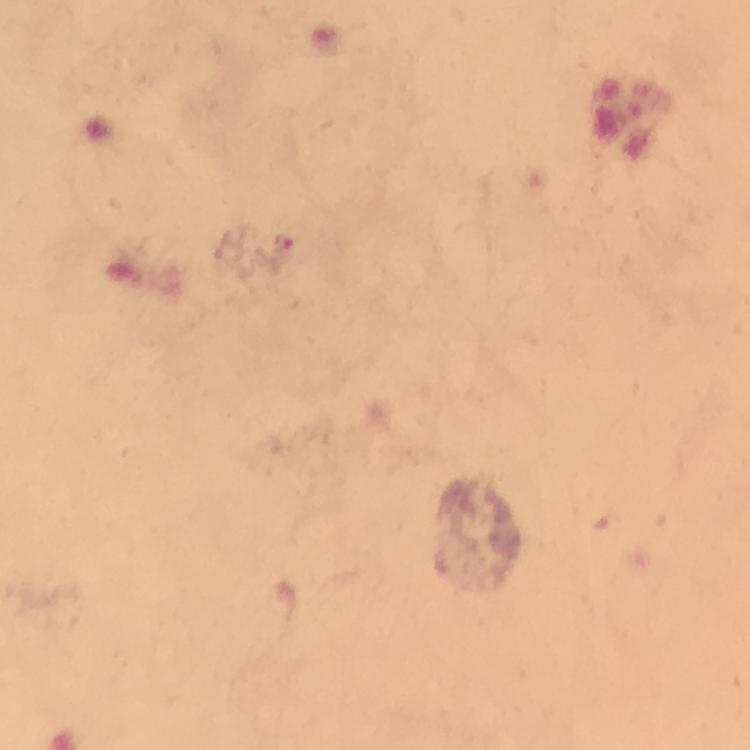

context = from a diagnostic examination for malaria
capture = smartphone photograph through a microscope
preparation = thick blood smear
magnification = 100x
cropped from = one field of view
image size = 750×750 pixels
malaria parasite locations = approximate object centers, in pixels from the top-left corner: (x=284, y=248)
stain = Giemsa
immersion oil = used